Report the malaria status of this cell.
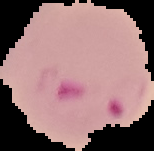
Parasitized.

Summary:
  - Preparation: thin blood smear
  - Image type: segmented cell region with the area outside set to black
  - Image size: 154×151 pixels